Point out each malaria parasite.
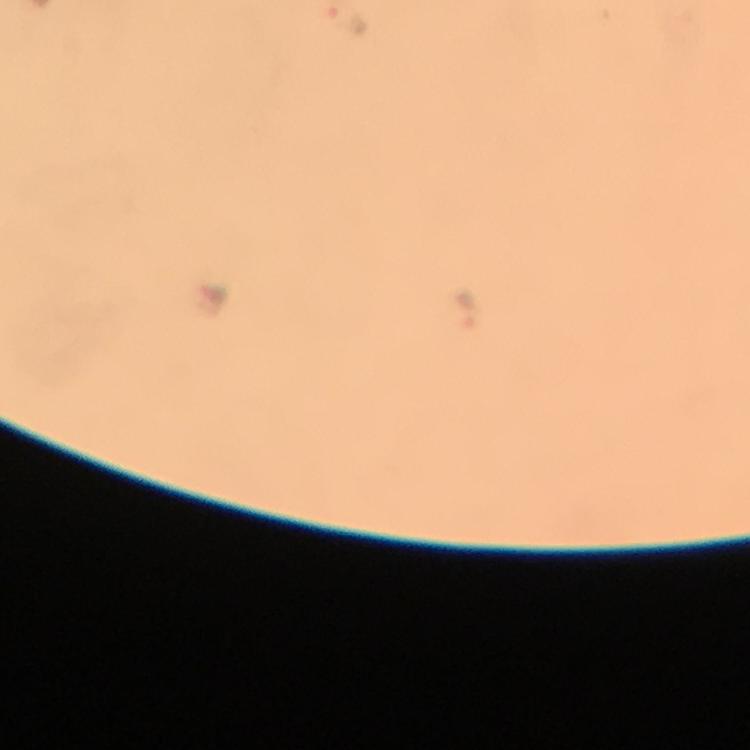
Approximate centers as (x, y) in pixels.
Malaria parasites: (349, 20), (466, 310).

Summary:
  - Capture: smartphone mounted on the microscope
  - Immersion oil: applied
  - Magnification: 100x
  - Context: from a diagnostic examination for malaria
  - Stain: Giemsa
  - Image size: 750×750 pixels
  - Preparation: thick blood film
  - Cropped from: one field of view